Name the blood parasite species.
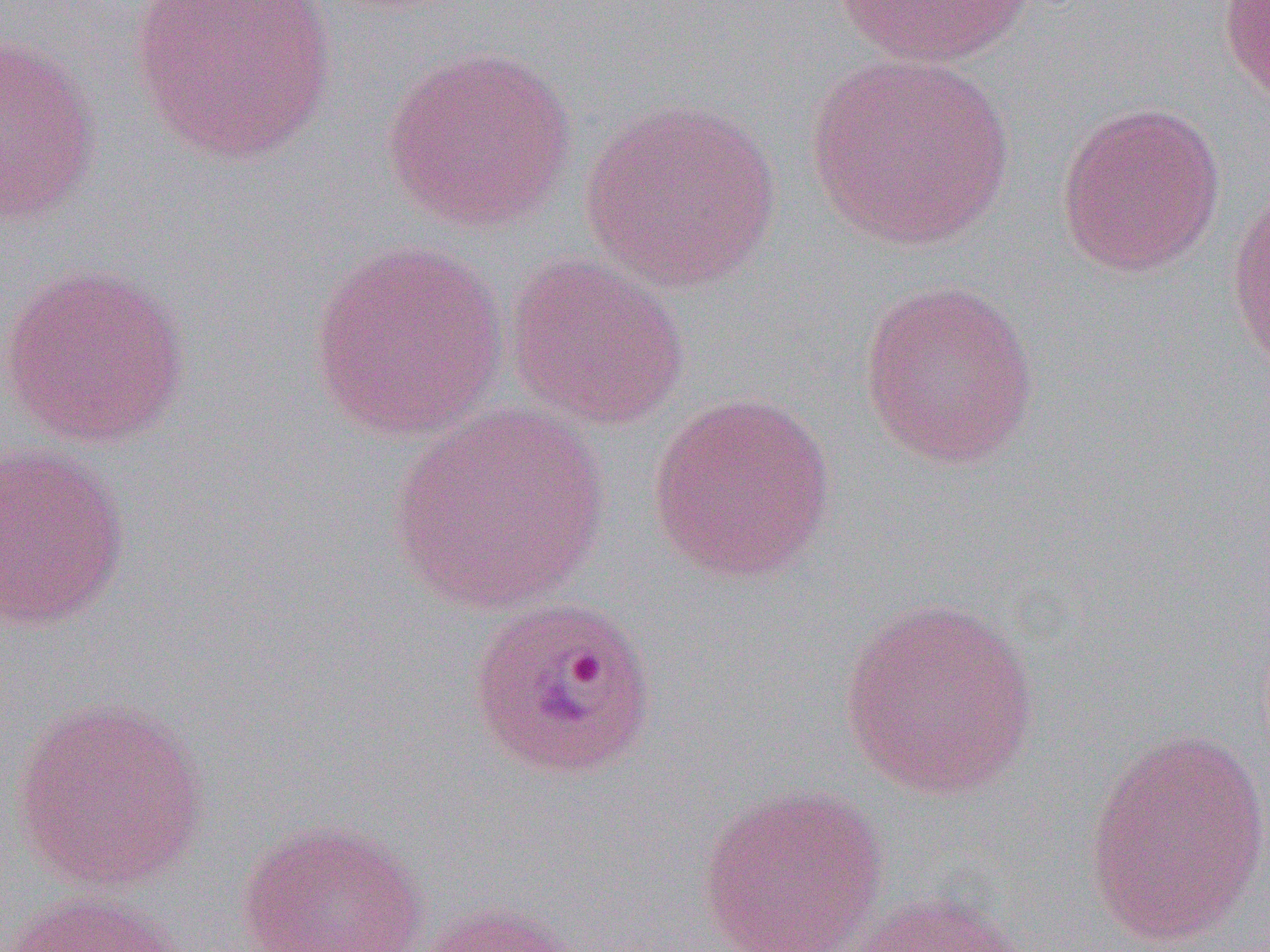
Plasmodium ovale.

Summary:
  - Coordinate format: approximate bounding boxes as named x1/y1/x2/y2 corners in pixels
  - Uninfected red blood cell locations: (x1=127, y1=0, x2=338, y2=166), (x1=833, y1=0, x2=1034, y2=68), (x1=1219, y1=0, x2=1270, y2=105), (x1=0, y1=34, x2=102, y2=226), (x1=381, y1=44, x2=579, y2=233), (x1=804, y1=53, x2=1018, y2=251), (x1=579, y1=99, x2=784, y2=292), (x1=1056, y1=101, x2=1226, y2=277), (x1=1226, y1=176, x2=1270, y2=380), (x1=308, y1=240, x2=509, y2=441), (x1=504, y1=252, x2=690, y2=430), (x1=0, y1=263, x2=193, y2=449), (x1=858, y1=279, x2=1040, y2=470), (x1=647, y1=391, x2=838, y2=584), (x1=388, y1=403, x2=613, y2=618), (x1=0, y1=441, x2=131, y2=632), (x1=839, y1=595, x2=1041, y2=800), (x1=9, y1=694, x2=212, y2=893), (x1=1081, y1=725, x2=1270, y2=951), (x1=695, y1=783, x2=890, y2=952), (x1=237, y1=818, x2=429, y2=952), (x1=5, y1=889, x2=189, y2=952), (x1=844, y1=890, x2=1029, y2=952), (x1=413, y1=900, x2=591, y2=952)
  - Plasmodium ovale-infected red blood cell locations: (x1=465, y1=595, x2=659, y2=781)
  - Preparation: thin blood smear
  - Image size: 1270×952 pixels
  - Modality: optical microscopy
  - Magnification: 1000x
  - Field of view: single